Identify the parasite.
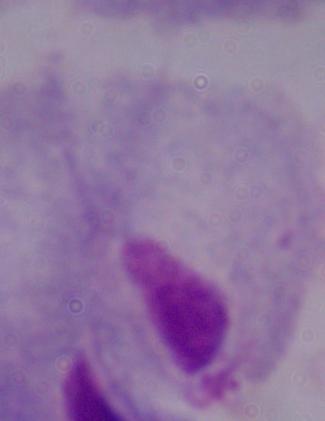
This is a trichomonad.

magnification: 1000x
modality: micrograph